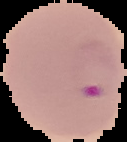

Image is 127×142 pixels. Malaria status: parasitized. From a thin blood film. The area outside the segmented cell region is set to black.